Give the position of every Plasmodium parasite visible.
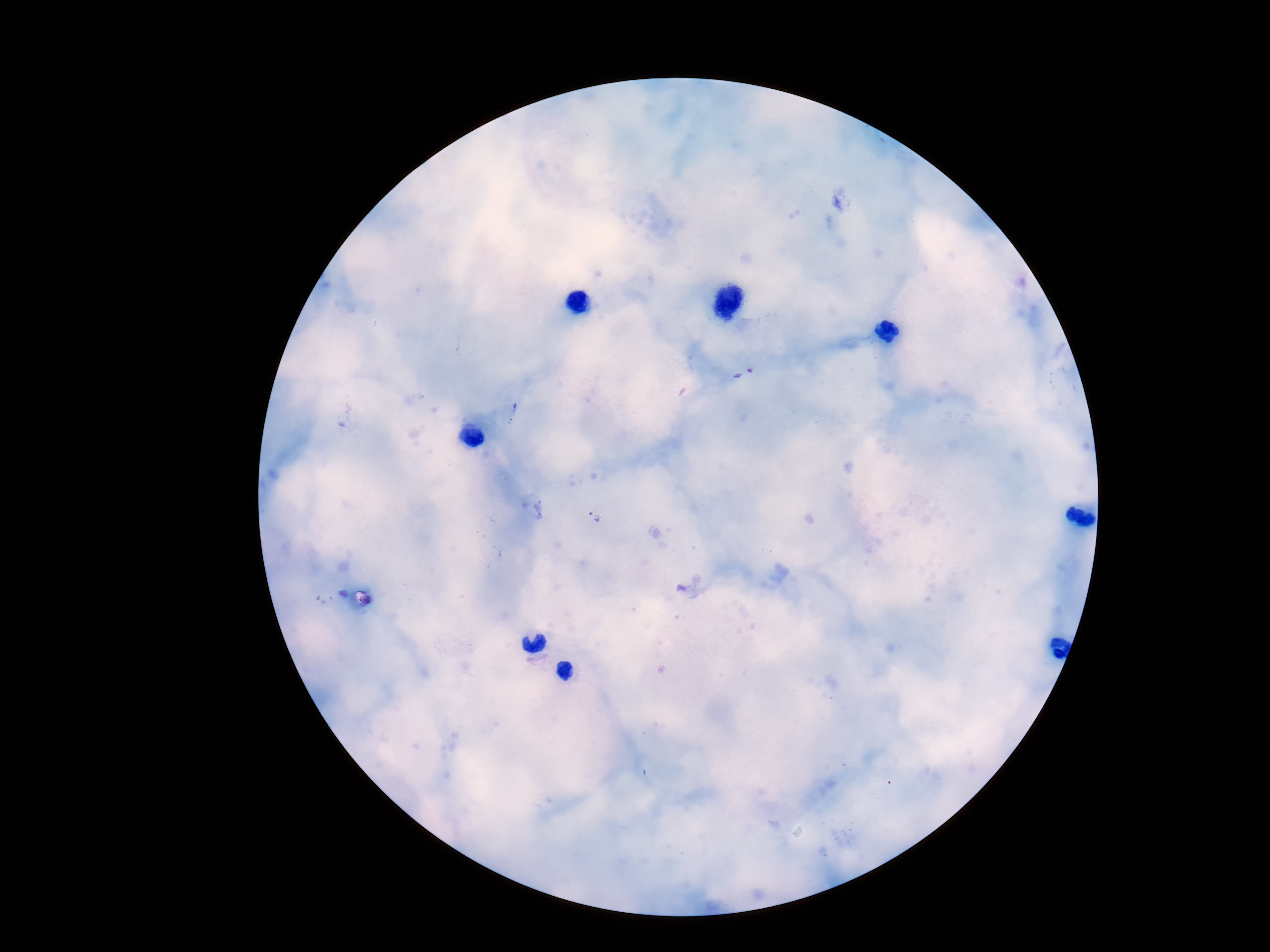
Approximate centers as [x, y] in pixels.
Plasmodium parasites: [744, 376], [511, 411], [595, 516].

magnification = 100x
image size = 1270×952 pixels
field of view = single
capture = smartphone camera through the microscope eyepiece
stain = Giemsa
patient malaria status = positive
preparation = thick blood smear